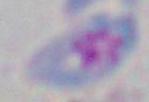
identification = Toxoplasma gondii
magnification = 1000x
modality = photomicrograph